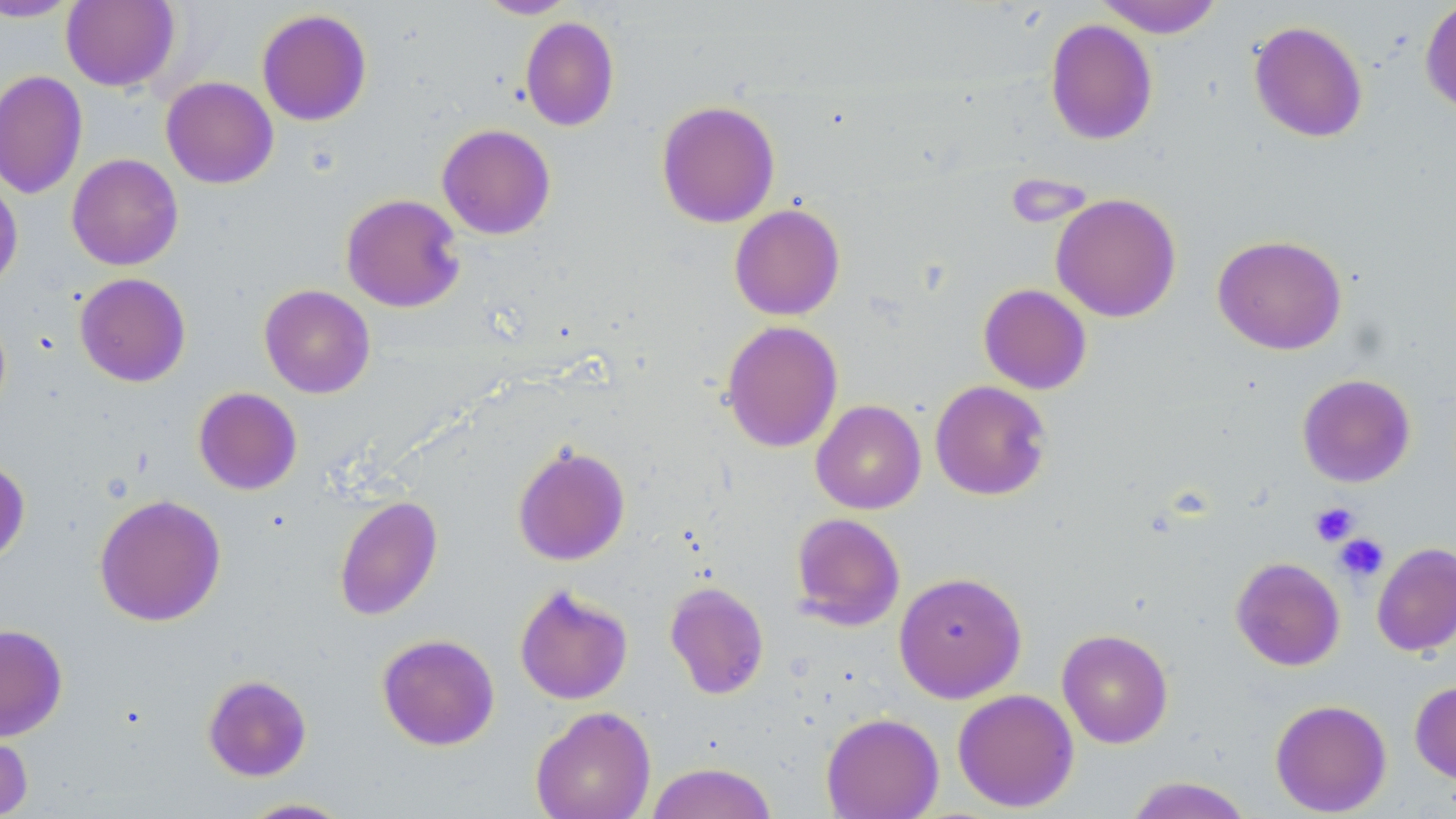
Summary:
  - Coordinate format: approximate bounding boxes as named x1/y1/x2/y2 corners in pixels
  - Platelet locations: (x1=1309, y1=502, x2=1360, y2=546), (x1=1333, y1=533, x2=1389, y2=583)
  - Uninfected red blood cell locations: (x1=476, y1=0, x2=578, y2=19), (x1=1094, y1=0, x2=1225, y2=38), (x1=1419, y1=0, x2=1456, y2=117), (x1=0, y1=1, x2=81, y2=22), (x1=61, y1=1, x2=179, y2=91), (x1=256, y1=8, x2=372, y2=126), (x1=519, y1=16, x2=620, y2=132), (x1=1044, y1=18, x2=1158, y2=145), (x1=1248, y1=20, x2=1368, y2=143), (x1=0, y1=70, x2=88, y2=200), (x1=161, y1=76, x2=279, y2=189), (x1=656, y1=100, x2=781, y2=228), (x1=437, y1=123, x2=556, y2=239), (x1=66, y1=154, x2=183, y2=271), (x1=0, y1=177, x2=23, y2=293), (x1=341, y1=193, x2=466, y2=313), (x1=1051, y1=193, x2=1181, y2=323), (x1=729, y1=203, x2=846, y2=320), (x1=1212, y1=234, x2=1347, y2=355), (x1=74, y1=273, x2=191, y2=387), (x1=259, y1=284, x2=375, y2=398), (x1=978, y1=284, x2=1092, y2=394), (x1=720, y1=321, x2=843, y2=453), (x1=1297, y1=374, x2=1416, y2=487), (x1=929, y1=380, x2=1052, y2=501), (x1=193, y1=387, x2=303, y2=495), (x1=811, y1=400, x2=926, y2=514), (x1=512, y1=443, x2=631, y2=566), (x1=0, y1=458, x2=31, y2=564), (x1=94, y1=494, x2=226, y2=627), (x1=333, y1=495, x2=443, y2=621), (x1=790, y1=513, x2=906, y2=631), (x1=1372, y1=542, x2=1456, y2=656), (x1=1231, y1=557, x2=1345, y2=671), (x1=893, y1=570, x2=1028, y2=703), (x1=664, y1=581, x2=769, y2=700), (x1=514, y1=584, x2=633, y2=705), (x1=0, y1=624, x2=68, y2=741), (x1=1057, y1=628, x2=1174, y2=748), (x1=377, y1=633, x2=500, y2=751), (x1=202, y1=674, x2=312, y2=781), (x1=1409, y1=680, x2=1456, y2=785), (x1=952, y1=688, x2=1079, y2=812), (x1=1270, y1=698, x2=1392, y2=816), (x1=530, y1=705, x2=656, y2=819), (x1=821, y1=712, x2=944, y2=818), (x1=0, y1=727, x2=33, y2=819), (x1=645, y1=761, x2=778, y2=819), (x1=1124, y1=776, x2=1254, y2=819), (x1=236, y1=797, x2=356, y2=818)
  - Slide-level diagnosis: no evidence of blood parasites
  - Preparation: thin blood smear
  - Magnification: 1000x
  - Stain: May-Grünwald-Giemsa
  - Field of view: single
  - Modality: light microscopy
  - Image size: 1456×819 pixels